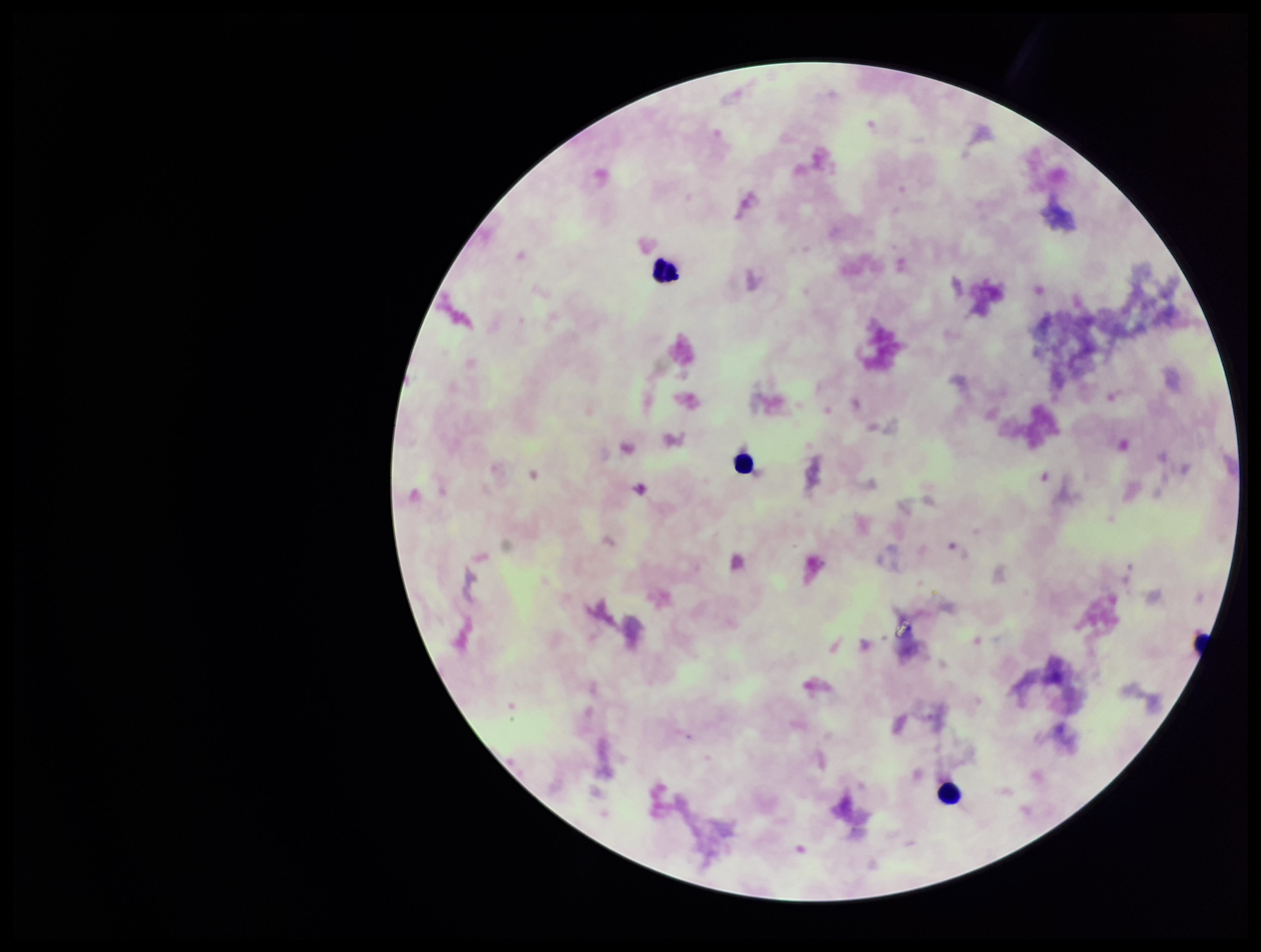

Summary:
  - Parasite count: 0
  - Capture: smartphone photograph through the microscope eyepiece
  - Preparation: thick smear
  - Leukocyte count: 3
  - Field of view: single
  - Image size: 1261×952 pixels
  - Patient malaria status: negative
  - Stain: Giemsa
  - Plasmodium parasites: none identified